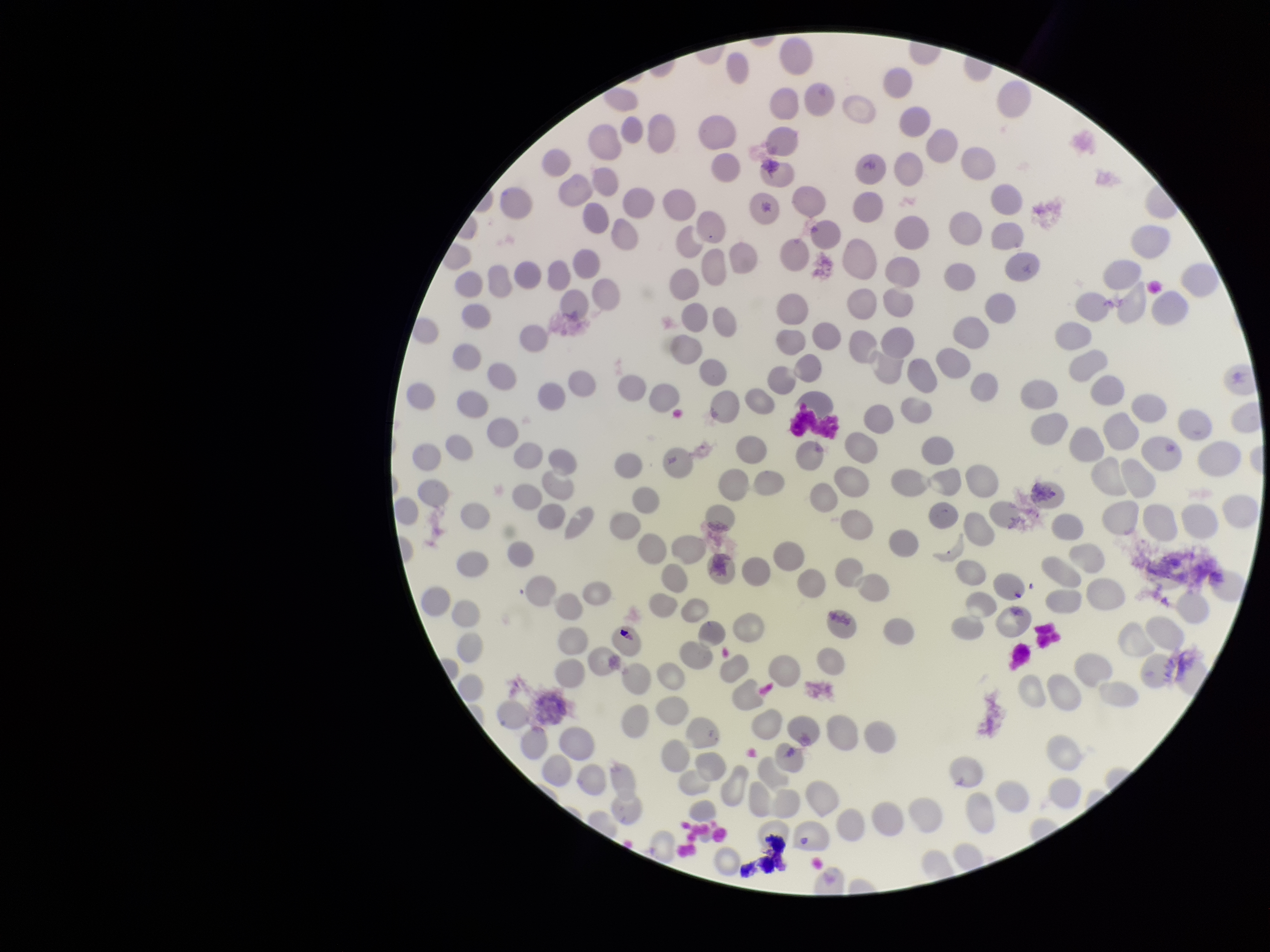

Summary:
  - Stain: Giemsa
  - Red blood cell count: 227
  - Preparation: thin
  - Patient malaria status: negative
  - Capture: smartphone photograph through the microscope eyepiece
  - Parasitized red blood cells: none seen
  - Image size: 1270×952 pixels
  - Parasitized red blood cell count: 0
  - Field of view: single